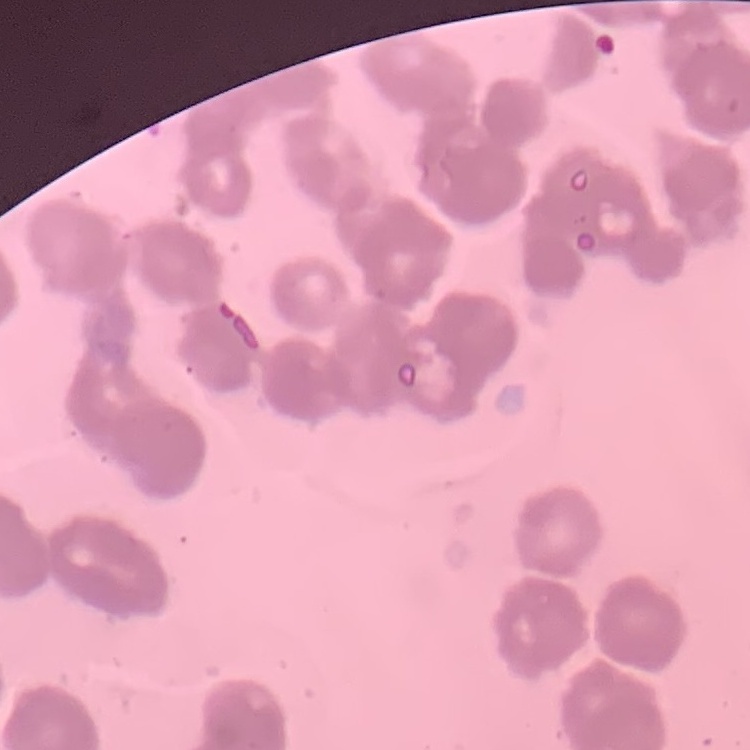
The erythrocytes show rouleaux formation. Thin peripheral smear. Field's or Giemsa stain. One tile cut from a larger photomicrograph.